Classify this cell by malaria status.
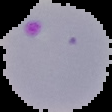

It is parasitized.

image size = 112×112 pixels
image type = segmented cell region on a black background
preparation = thin blood smear